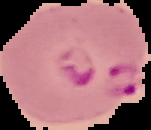
image_type: segmented cell region with the area outside set to black
malaria_status: parasitized
preparation: thin blood smear
image_size: 151×130 pixels